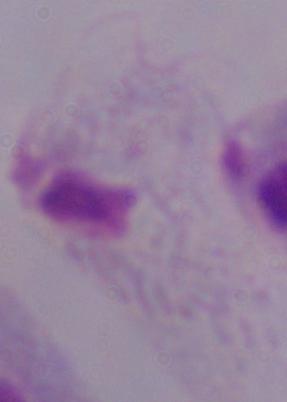
identification: trichomonad
modality: photomicrograph
magnification: 1000x